Classify this cell by malaria status.
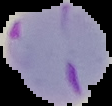

It is parasitized.

image size = 112×106 pixels
preparation = thin blood film
image type = cell region segmented out of the field of view; surrounding area masked to black